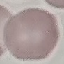 Malaria status: uninfected. Automatically extracted cell patch, resized to 64 × 64 pixels. Thin smear of blood. Photographed with a smartphone camera at the microscope eyepiece. Giemsa-stained preparation.